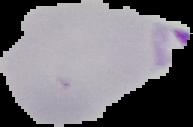

Summary:
  - Preparation: thin blood film
  - Image size: 193×127 pixels
  - Image type: cell region segmented out of the field of view; surrounding area masked to black
  - Result: malaria parasites identified